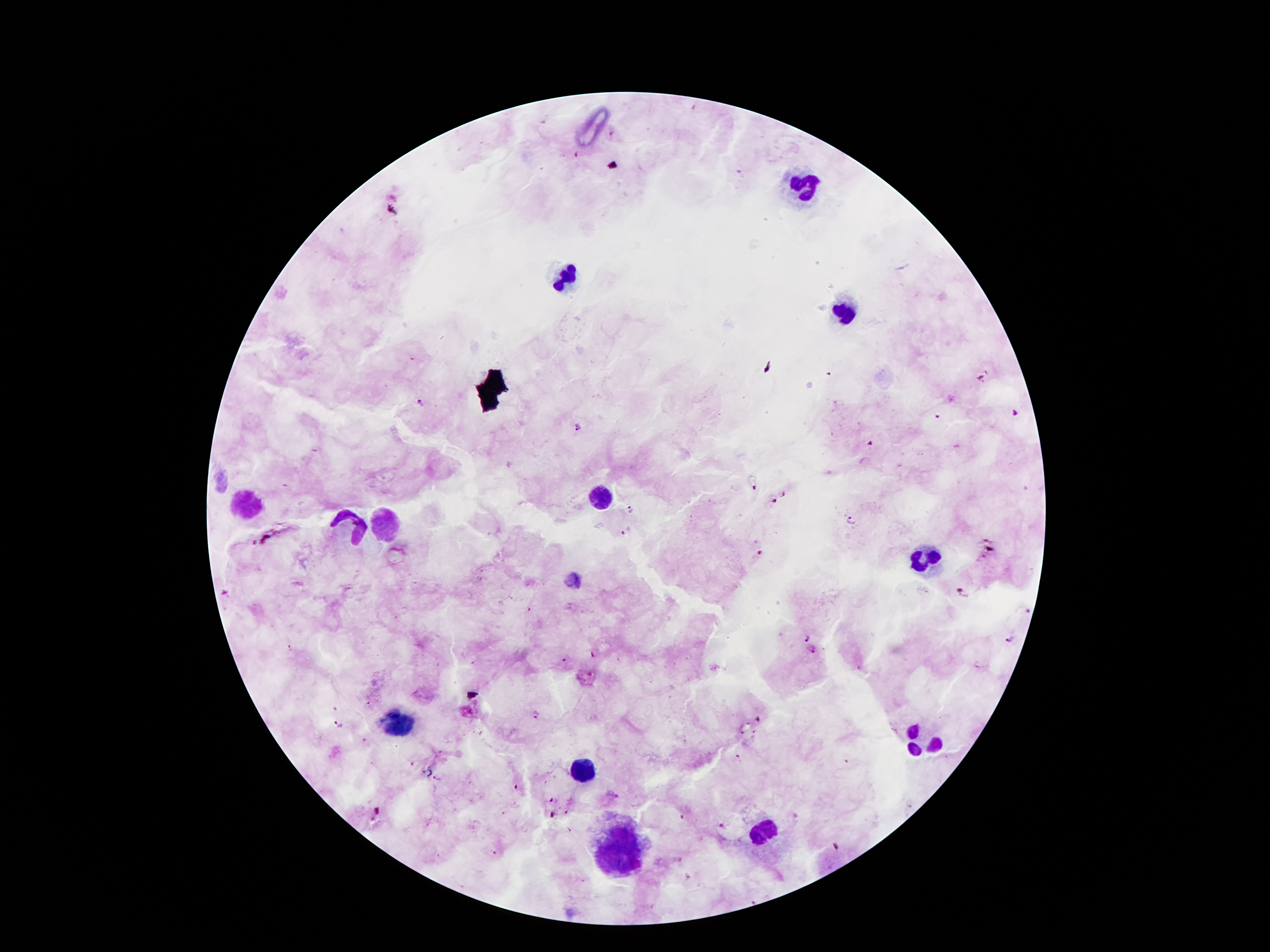

Approximate centers as [x, y] in pixels. Leukocyte locations: [802, 186], [565, 272], [846, 312], [601, 497], [246, 502], [384, 518], [351, 528], [926, 560], [401, 721], [922, 738], [582, 770], [766, 829], [620, 846]. Plasmodium parasite locations: [421, 404], [938, 417], [580, 425], [786, 494], [775, 501], [632, 510], [850, 518], [628, 532], [761, 553], [1028, 611], [806, 639], [1010, 639], [814, 651], [536, 713], [338, 724], [722, 826]. Thick blood smear. Giemsa stain. Patient malaria status: positive for Plasmodium falciparum. One field from this slide. Smartphone photograph taken through the microscope eyepiece. Image is 1270×952 pixels. 100x magnification.